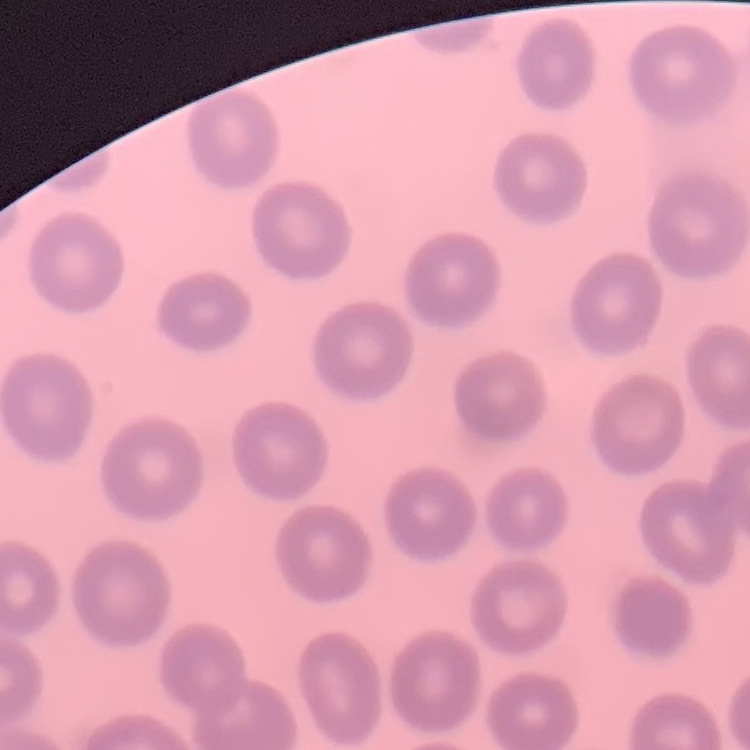
Summary:
  - Red blood cell morphology: no rouleaux formation
  - Preparation: thin blood smear
  - Stain: Field's or Giemsa
  - Image type: one tile cut from a larger photomicrograph